Classify this cell by malaria status.
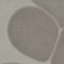

Uninfected.

Summary:
  - Image type: cell patch, automatically extracted from a larger field of view and resized to 64 × 64 pixels
  - Stain: Giemsa
  - Preparation: thin smear
  - Capture: smartphone through the microscope eyepiece